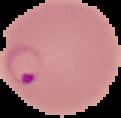

The area outside the segmented cell region is set to black. Malaria status: parasitized. Image is 121×118 pixels. From a thin blood film.